Locate every Plasmodium falciparum-infected red blood cell.
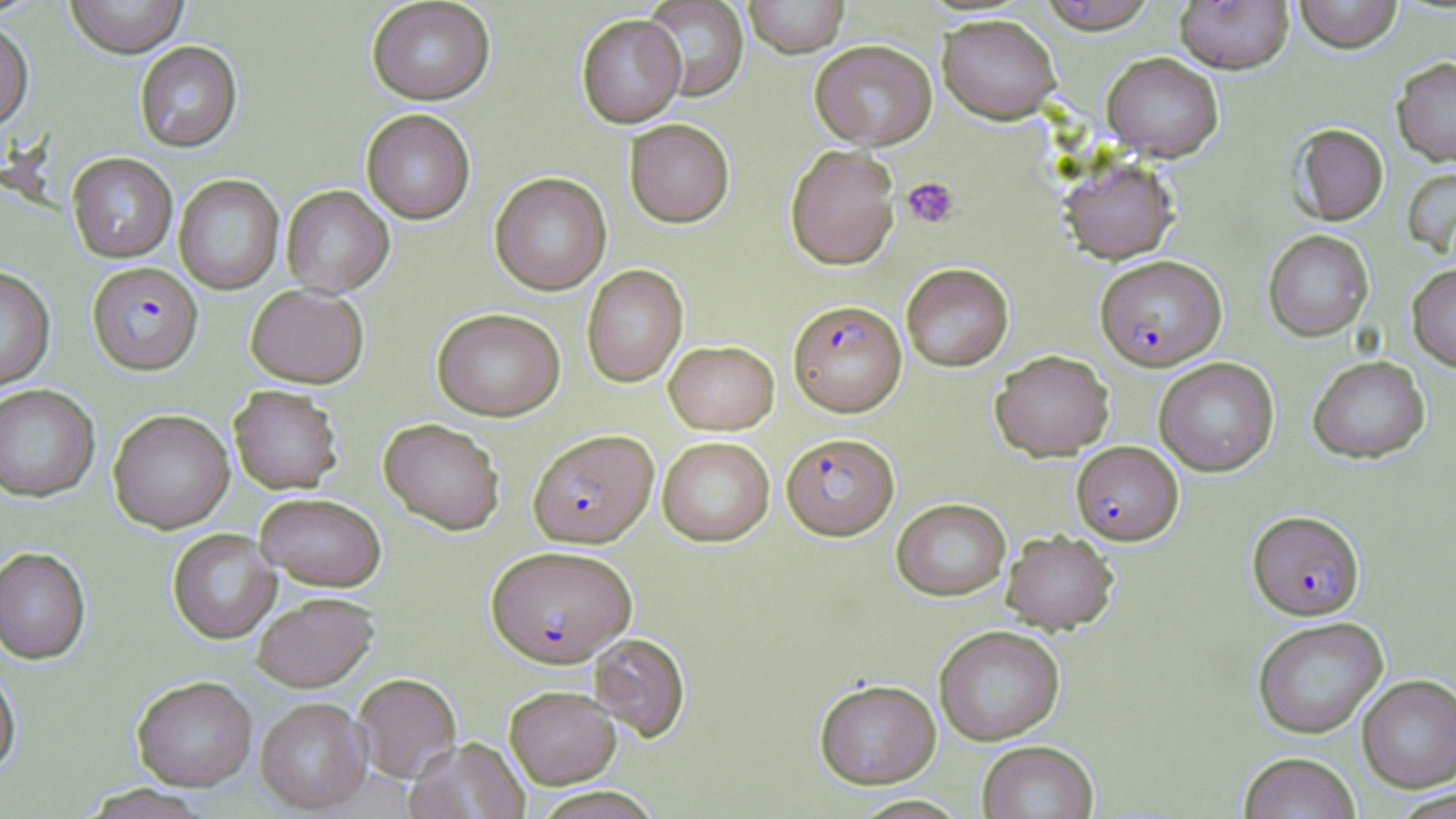
Approximate bounding boxes as [x1, y1, x2, y2] in pixels.
Plasmodium falciparum-infected red blood cells: [1096, 255, 1226, 370], [87, 262, 202, 374], [789, 299, 907, 417], [528, 429, 658, 547], [781, 432, 900, 540], [1071, 441, 1183, 544], [1248, 510, 1365, 619], [486, 545, 636, 668].

slide-level diagnosis = Plasmodium falciparum
field of view = single
image size = 1456×819 pixels
uninfected red blood cell locations = approximate bounding boxes as [x1, y1, x2, y2] in pixels: [64, 0, 189, 58], [366, 0, 496, 105], [642, 0, 749, 102], [744, 0, 849, 58], [1037, 0, 1159, 33], [1174, 0, 1294, 73], [1293, 0, 1402, 52], [577, 14, 686, 128], [938, 14, 1061, 124], [0, 18, 34, 132], [810, 40, 937, 149], [134, 41, 242, 152], [1102, 52, 1224, 162], [1391, 57, 1456, 166], [361, 109, 475, 223], [624, 118, 735, 228], [1289, 123, 1388, 225], [785, 144, 900, 269], [67, 152, 177, 262], [1058, 157, 1179, 265], [1401, 166, 1456, 259], [489, 171, 612, 295], [173, 174, 284, 295], [282, 185, 394, 297], [1263, 230, 1374, 341], [901, 263, 1013, 371], [1407, 263, 1456, 372], [581, 264, 688, 388], [0, 267, 55, 390], [246, 284, 369, 387], [432, 308, 566, 420], [664, 340, 779, 434], [990, 349, 1114, 460], [1307, 355, 1431, 463], [1154, 357, 1279, 476], [0, 384, 100, 502], [229, 385, 343, 494], [108, 409, 235, 533], [378, 418, 506, 535], [657, 436, 774, 546], [255, 492, 387, 591], [891, 497, 1011, 601], [168, 528, 280, 643], [1001, 529, 1119, 635], [0, 547, 91, 664], [252, 592, 379, 691], [1252, 616, 1388, 739], [934, 625, 1065, 745], [588, 632, 691, 741], [0, 662, 21, 778], [353, 673, 461, 783], [1356, 674, 1456, 792], [132, 676, 257, 791], [814, 678, 940, 788], [504, 685, 620, 787], [255, 697, 371, 814], [405, 737, 529, 819], [977, 740, 1098, 819], [1238, 752, 1361, 818], [79, 785, 215, 819], [527, 787, 664, 818], [850, 795, 972, 818]
modality = optical microscopy
preparation = thin blood film
stain = May-Grünwald-Giemsa
platelet locations = approximate bounding boxes as [x1, y1, x2, y2] in pixels: [902, 176, 959, 229]
magnification = 1000x